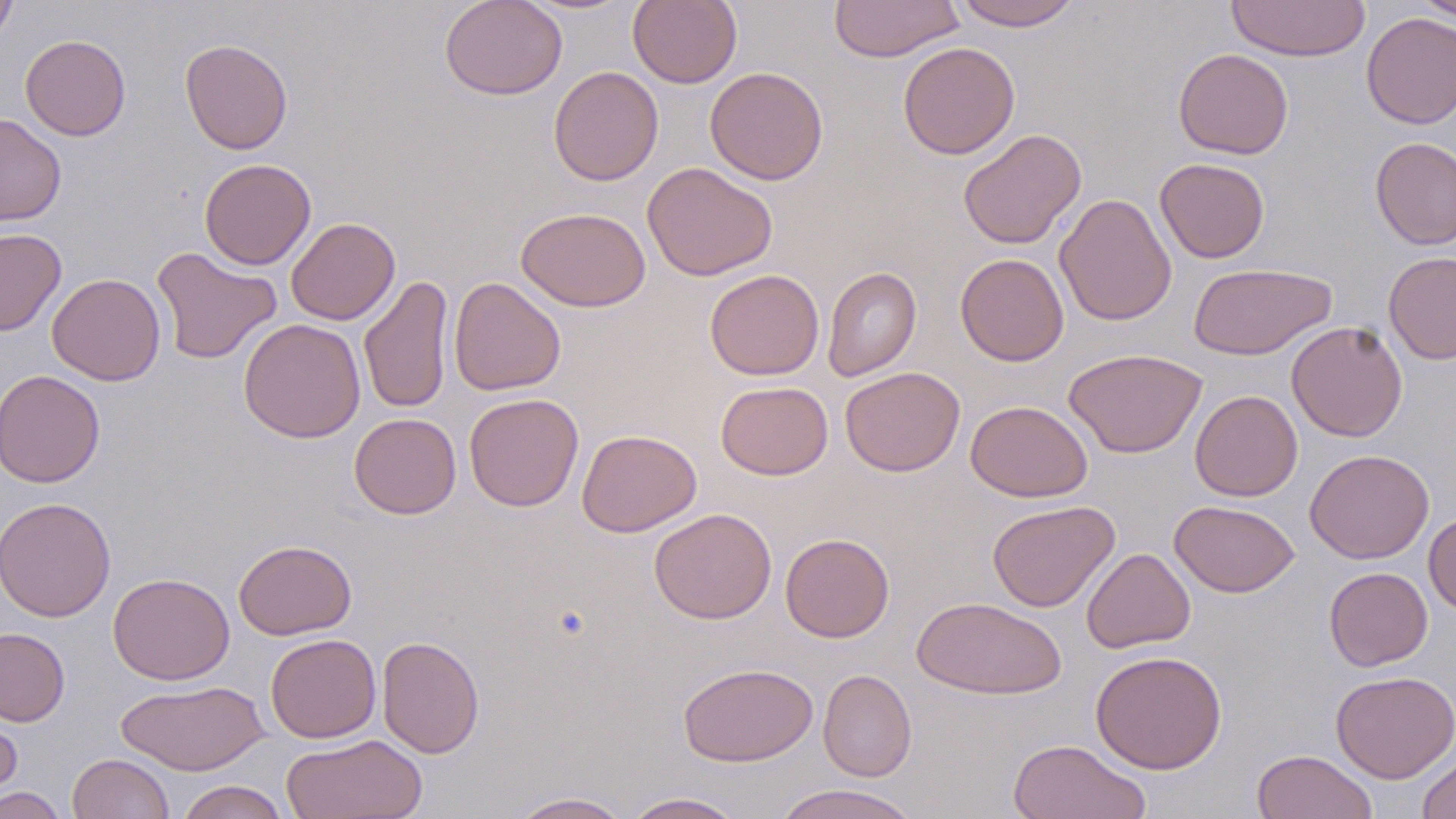
slide_level_diagnosis: negative for blood parasites
uninfected_red_blood_cell_locations: 'approximate bounding boxes as named x1/y1/x2/y2 corners in pixels: (x1=439, y1=0, x2=568, y2=100), (x1=628, y1=0, x2=742, y2=88), (x1=828, y1=0, x2=965, y2=63), (x1=953, y1=0, x2=1083, y2=31), (x1=1413, y1=0, x2=1456, y2=23), (x1=0, y1=1, x2=18, y2=48), (x1=1226, y1=1, x2=1370, y2=61), (x1=1361, y1=12, x2=1456, y2=129), (x1=20, y1=34, x2=131, y2=141), (x1=180, y1=39, x2=293, y2=154), (x1=897, y1=41, x2=1020, y2=160), (x1=1173, y1=48, x2=1294, y2=160), (x1=548, y1=66, x2=664, y2=186), (x1=704, y1=66, x2=829, y2=185), (x1=0, y1=113, x2=67, y2=226), (x1=958, y1=129, x2=1086, y2=249), (x1=1370, y1=136, x2=1456, y2=250), (x1=199, y1=158, x2=316, y2=270), (x1=1154, y1=158, x2=1270, y2=263), (x1=642, y1=161, x2=778, y2=281), (x1=1055, y1=193, x2=1177, y2=326), (x1=516, y1=207, x2=651, y2=311), (x1=285, y1=217, x2=400, y2=325), (x1=0, y1=228, x2=67, y2=336), (x1=151, y1=246, x2=282, y2=364), (x1=955, y1=252, x2=1069, y2=366), (x1=1383, y1=252, x2=1456, y2=364), (x1=1188, y1=263, x2=1335, y2=360), (x1=822, y1=265, x2=921, y2=382), (x1=704, y1=269, x2=824, y2=380), (x1=47, y1=273, x2=165, y2=385), (x1=359, y1=275, x2=454, y2=414), (x1=448, y1=277, x2=566, y2=396), (x1=238, y1=319, x2=366, y2=443), (x1=1286, y1=321, x2=1408, y2=442), (x1=1064, y1=348, x2=1207, y2=458), (x1=840, y1=366, x2=965, y2=477), (x1=0, y1=369, x2=105, y2=488), (x1=715, y1=381, x2=833, y2=480), (x1=1190, y1=389, x2=1303, y2=501), (x1=463, y1=393, x2=583, y2=512), (x1=965, y1=400, x2=1093, y2=502), (x1=349, y1=413, x2=461, y2=519), (x1=576, y1=429, x2=702, y2=536), (x1=1305, y1=448, x2=1434, y2=563), (x1=0, y1=496, x2=116, y2=622), (x1=987, y1=500, x2=1120, y2=612), (x1=1169, y1=500, x2=1300, y2=597), (x1=648, y1=507, x2=777, y2=624), (x1=1423, y1=513, x2=1456, y2=616), (x1=780, y1=532, x2=895, y2=642), (x1=233, y1=539, x2=357, y2=640), (x1=1081, y1=547, x2=1195, y2=653), (x1=1324, y1=567, x2=1432, y2=671), (x1=108, y1=572, x2=234, y2=684), (x1=910, y1=596, x2=1066, y2=700), (x1=0, y1=627, x2=70, y2=727), (x1=265, y1=634, x2=381, y2=743), (x1=377, y1=635, x2=485, y2=759), (x1=1089, y1=649, x2=1228, y2=774), (x1=678, y1=662, x2=818, y2=767), (x1=818, y1=668, x2=916, y2=782), (x1=1330, y1=670, x2=1456, y2=783), (x1=115, y1=679, x2=270, y2=776), (x1=0, y1=696, x2=24, y2=808), (x1=281, y1=733, x2=428, y2=819), (x1=1007, y1=739, x2=1151, y2=819), (x1=1251, y1=749, x2=1377, y2=819), (x1=1417, y1=752, x2=1456, y2=819), (x1=68, y1=753, x2=174, y2=818), (x1=176, y1=780, x2=291, y2=819), (x1=772, y1=784, x2=921, y2=819), (x1=0, y1=787, x2=69, y2=818), (x1=507, y1=792, x2=633, y2=819), (x1=620, y1=792, x2=747, y2=818)'
field_of_view: single
stain: May-Grünwald-Giemsa
modality: optical microscopy
preparation: thin blood smear
magnification: 1000x
image_size: 1456×819 pixels